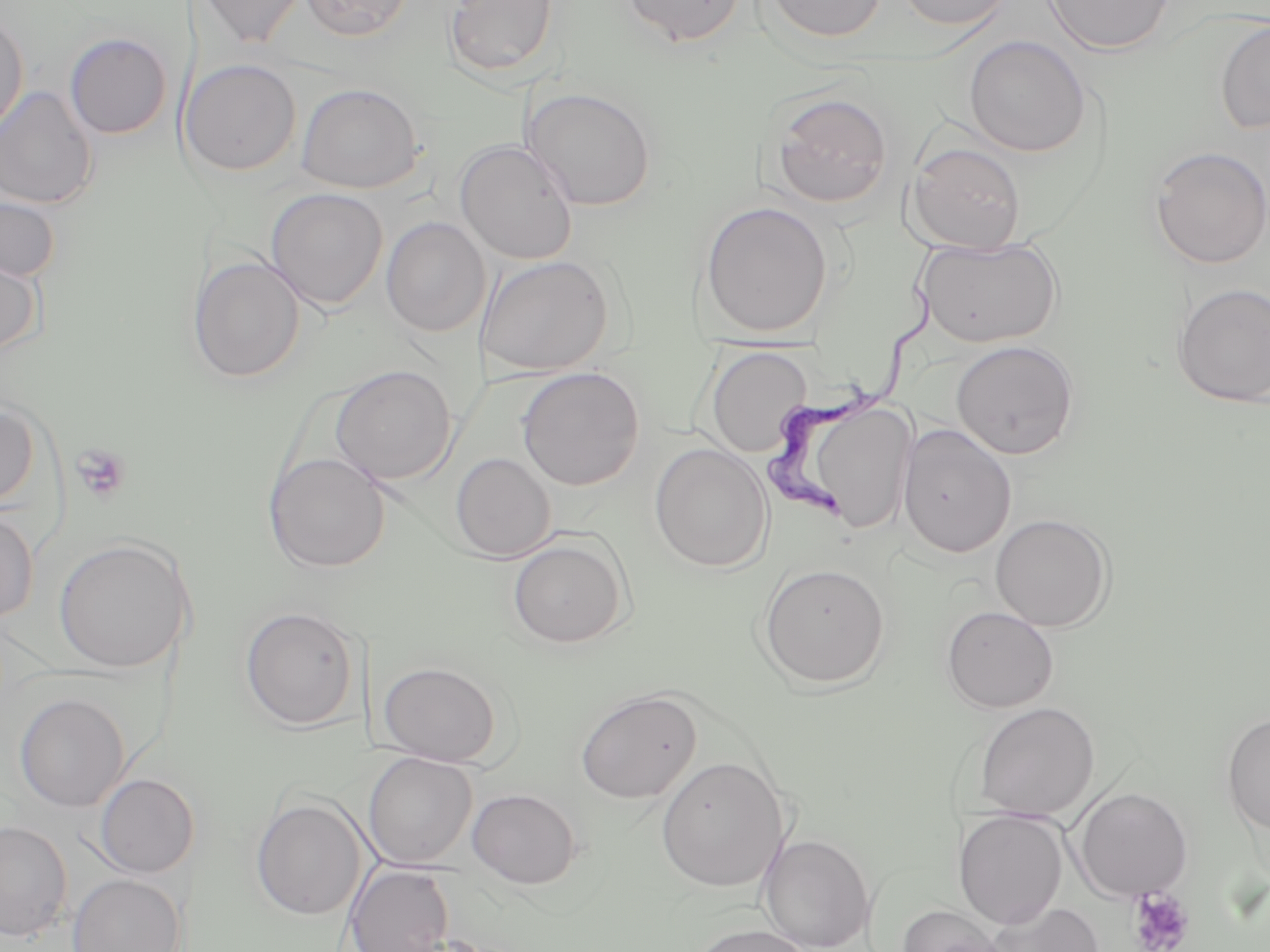
Approximate bounding boxes as named x1/y1/x2/y2 corners in pixels. Uninfected red blood cell locations: (x1=192, y1=0, x2=308, y2=50), (x1=299, y1=0, x2=414, y2=42), (x1=445, y1=0, x2=559, y2=79), (x1=621, y1=0, x2=746, y2=47), (x1=763, y1=0, x2=887, y2=44), (x1=894, y1=0, x2=1016, y2=31), (x1=1041, y1=0, x2=1175, y2=56), (x1=0, y1=12, x2=29, y2=136), (x1=1215, y1=19, x2=1270, y2=134), (x1=64, y1=32, x2=172, y2=140), (x1=964, y1=35, x2=1090, y2=157), (x1=179, y1=58, x2=301, y2=177), (x1=296, y1=82, x2=424, y2=194), (x1=0, y1=85, x2=98, y2=210), (x1=522, y1=87, x2=656, y2=211), (x1=769, y1=90, x2=893, y2=209), (x1=454, y1=140, x2=579, y2=264), (x1=907, y1=141, x2=1026, y2=254), (x1=1149, y1=146, x2=1270, y2=269), (x1=265, y1=187, x2=389, y2=310), (x1=0, y1=195, x2=61, y2=283), (x1=699, y1=200, x2=834, y2=337), (x1=381, y1=217, x2=490, y2=336), (x1=915, y1=235, x2=1063, y2=348), (x1=0, y1=252, x2=43, y2=357), (x1=475, y1=254, x2=616, y2=376), (x1=188, y1=255, x2=306, y2=383), (x1=1172, y1=283, x2=1270, y2=408), (x1=950, y1=340, x2=1079, y2=460), (x1=706, y1=346, x2=812, y2=457), (x1=330, y1=364, x2=457, y2=486), (x1=516, y1=367, x2=645, y2=490), (x1=812, y1=394, x2=928, y2=532), (x1=0, y1=401, x2=41, y2=509), (x1=898, y1=423, x2=1016, y2=558), (x1=649, y1=443, x2=774, y2=573), (x1=263, y1=452, x2=391, y2=573), (x1=450, y1=452, x2=556, y2=562), (x1=0, y1=509, x2=38, y2=623), (x1=989, y1=513, x2=1114, y2=631), (x1=507, y1=536, x2=630, y2=648), (x1=53, y1=537, x2=192, y2=673), (x1=758, y1=563, x2=890, y2=690), (x1=941, y1=605, x2=1059, y2=713), (x1=240, y1=606, x2=360, y2=730), (x1=378, y1=661, x2=502, y2=766), (x1=575, y1=688, x2=702, y2=803), (x1=14, y1=693, x2=130, y2=811), (x1=972, y1=701, x2=1099, y2=820), (x1=1221, y1=713, x2=1270, y2=834), (x1=362, y1=752, x2=478, y2=869), (x1=656, y1=756, x2=789, y2=892), (x1=94, y1=773, x2=199, y2=878), (x1=466, y1=787, x2=582, y2=888), (x1=1073, y1=787, x2=1193, y2=902), (x1=250, y1=796, x2=368, y2=921), (x1=953, y1=809, x2=1069, y2=928), (x1=0, y1=821, x2=72, y2=942), (x1=759, y1=833, x2=875, y2=951), (x1=345, y1=863, x2=455, y2=952), (x1=68, y1=874, x2=186, y2=952), (x1=985, y1=900, x2=1104, y2=952), (x1=897, y1=905, x2=1009, y2=952), (x1=688, y1=923, x2=815, y2=952). Trypanosoma brucei locations: (x1=762, y1=285, x2=933, y2=531). Platelet locations: (x1=70, y1=444, x2=132, y2=503), (x1=1127, y1=887, x2=1194, y2=952). Slide-level diagnosis: Trypanosoma brucei. One field of a larger specimen. Light microscopy. Captured at 1000x magnification. May-Grünwald-Giemsa-stained preparation. Image is 1270×952 pixels. Thin blood smear.